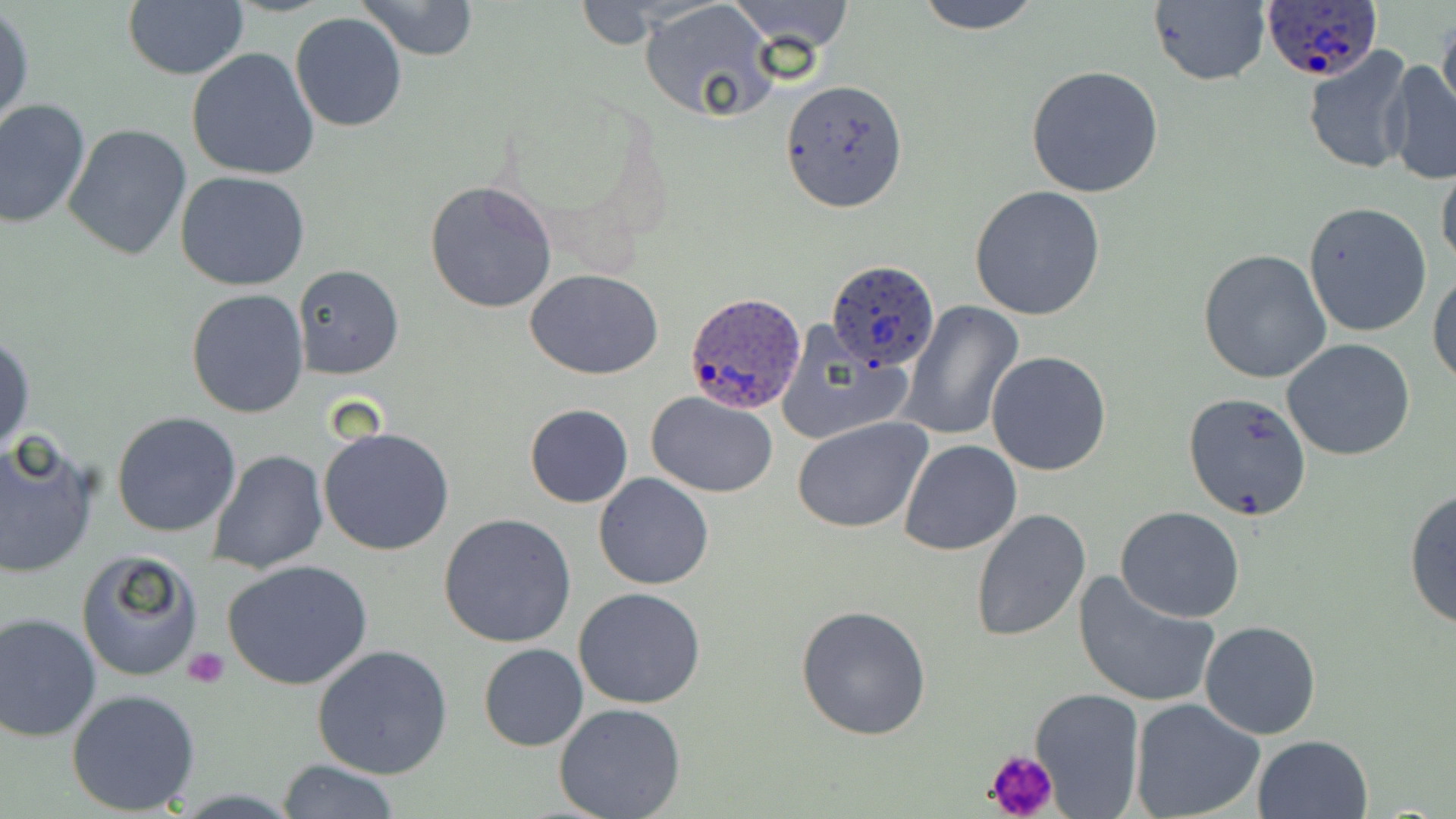

Summary:
  - Coordinate format: approximate bounding boxes as [x1, y1, x2, y2] in pixels
  - Uninfected red blood cell locations: [354, 0, 479, 62], [730, 0, 853, 52], [912, 0, 1044, 32], [122, 1, 248, 81], [1148, 1, 1270, 87], [639, 2, 779, 123], [0, 7, 34, 133], [290, 11, 409, 132], [1437, 11, 1456, 123], [1300, 45, 1416, 175], [187, 47, 320, 180], [1379, 57, 1456, 184], [1025, 65, 1164, 198], [778, 79, 908, 213], [0, 99, 91, 230], [64, 123, 192, 260], [1436, 161, 1456, 273], [176, 171, 310, 291], [425, 180, 558, 314], [969, 185, 1108, 322], [1303, 201, 1433, 338], [1198, 248, 1332, 382], [294, 265, 404, 379], [526, 269, 662, 379], [1429, 269, 1456, 386], [186, 288, 310, 417], [899, 302, 1024, 442], [773, 320, 911, 447], [0, 334, 35, 459], [1283, 338, 1416, 461], [986, 350, 1112, 477], [646, 392, 778, 498], [1183, 392, 1311, 522], [525, 405, 632, 508], [111, 412, 242, 538], [792, 417, 932, 533], [318, 425, 457, 557], [0, 435, 100, 578], [897, 439, 1022, 555], [206, 450, 329, 574], [592, 473, 714, 590], [1403, 487, 1456, 631], [1116, 507, 1245, 623], [970, 509, 1091, 644], [439, 513, 577, 649], [74, 547, 204, 683], [222, 558, 374, 690], [1070, 571, 1221, 709], [574, 586, 706, 709], [794, 604, 932, 741], [0, 613, 101, 743], [1198, 620, 1322, 739], [313, 643, 454, 779], [477, 643, 588, 752], [66, 687, 200, 815], [1028, 688, 1146, 817], [1131, 698, 1266, 819], [553, 702, 687, 819], [1251, 734, 1374, 819], [278, 758, 401, 817]
  - Platelet locations: [182, 646, 229, 689], [984, 747, 1059, 819]
  - Plasmodium ovale-infected red blood cell locations: [1261, 0, 1382, 83], [825, 259, 939, 371], [684, 290, 805, 415]
  - Slide-level diagnosis: Plasmodium ovale
  - Preparation: thin blood film
  - Image size: 1456×819 pixels
  - Field of view: one of a larger specimen
  - Stain: May-Grünwald-Giemsa
  - Modality: optical microscopy
  - Magnification: 1000x